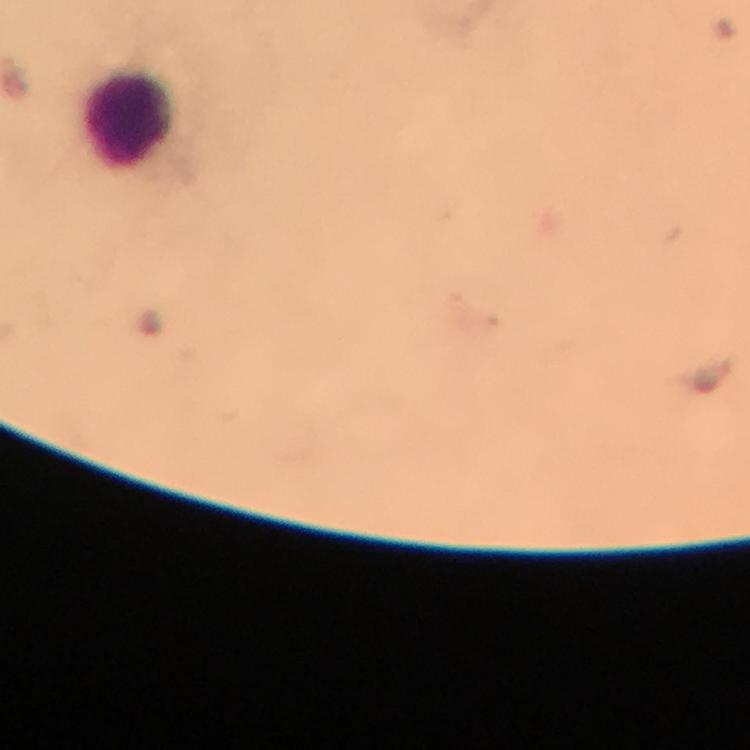
Approximate centers as [x, y] in pixels.
Summary:
  - Leukocyte locations: [127, 122]
  - Immersion oil: applied
  - Capture: smartphone camera through the microscope
  - Stain: Giemsa
  - Cropped from: a single field of view
  - Magnification: 100x
  - Context: from a malaria diagnostic workup
  - Image size: 750×750 pixels
  - Plasmodium parasites: none seen
  - Preparation: thick blood smear